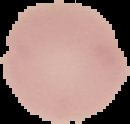

image_type: segmented cell region with the area outside set to black
malaria_status: uninfected
image_size: 130×124 pixels
preparation: thin blood smear